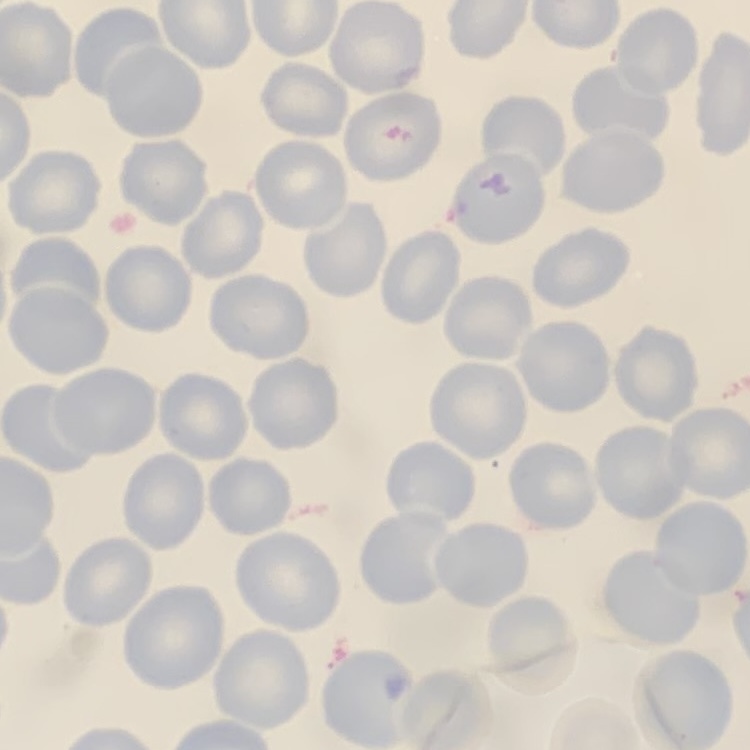

Summary:
  - Erythrocyte morphology: no rouleaux formation
  - Image type: square crop of a larger photomicrograph
  - Stain: Field's or Giemsa
  - Preparation: thin peripheral smear